Classify this cell by malaria status.
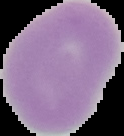
It is uninfected.

Summary:
  - Image type: segmented cell region with the area outside set to black
  - Image size: 124×136 pixels
  - Preparation: thin blood smear